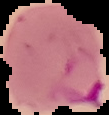

Summary:
  - Image type: segmented cell region on a black background
  - Preparation: thin blood smear
  - Image size: 109×115 pixels
  - Malaria status: parasitized